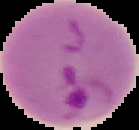 Image is 139×130 pixels. From a thin blood film. Cell region segmented out of the field of view; the surrounding area is masked to black. Malaria status: parasitized.